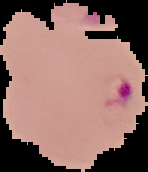
image size = 148×172 pixels
result = Plasmodium parasites detected
image type = segmented cell region with the area outside set to black
preparation = thin blood smear